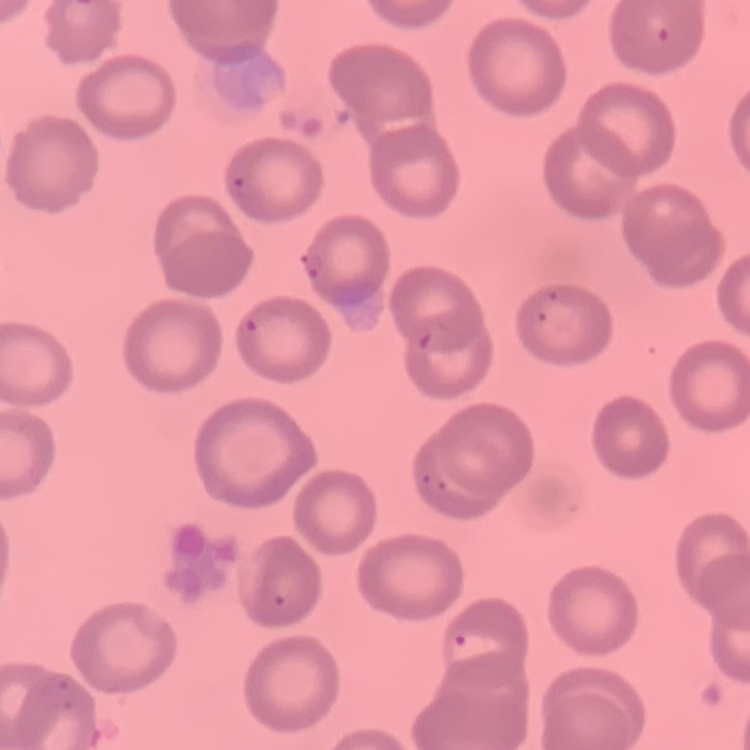

erythrocyte morphology = no rouleaux formation
preparation = thin peripheral smear
stain = Field's or Giemsa
image type = one tile cut from a larger photomicrograph